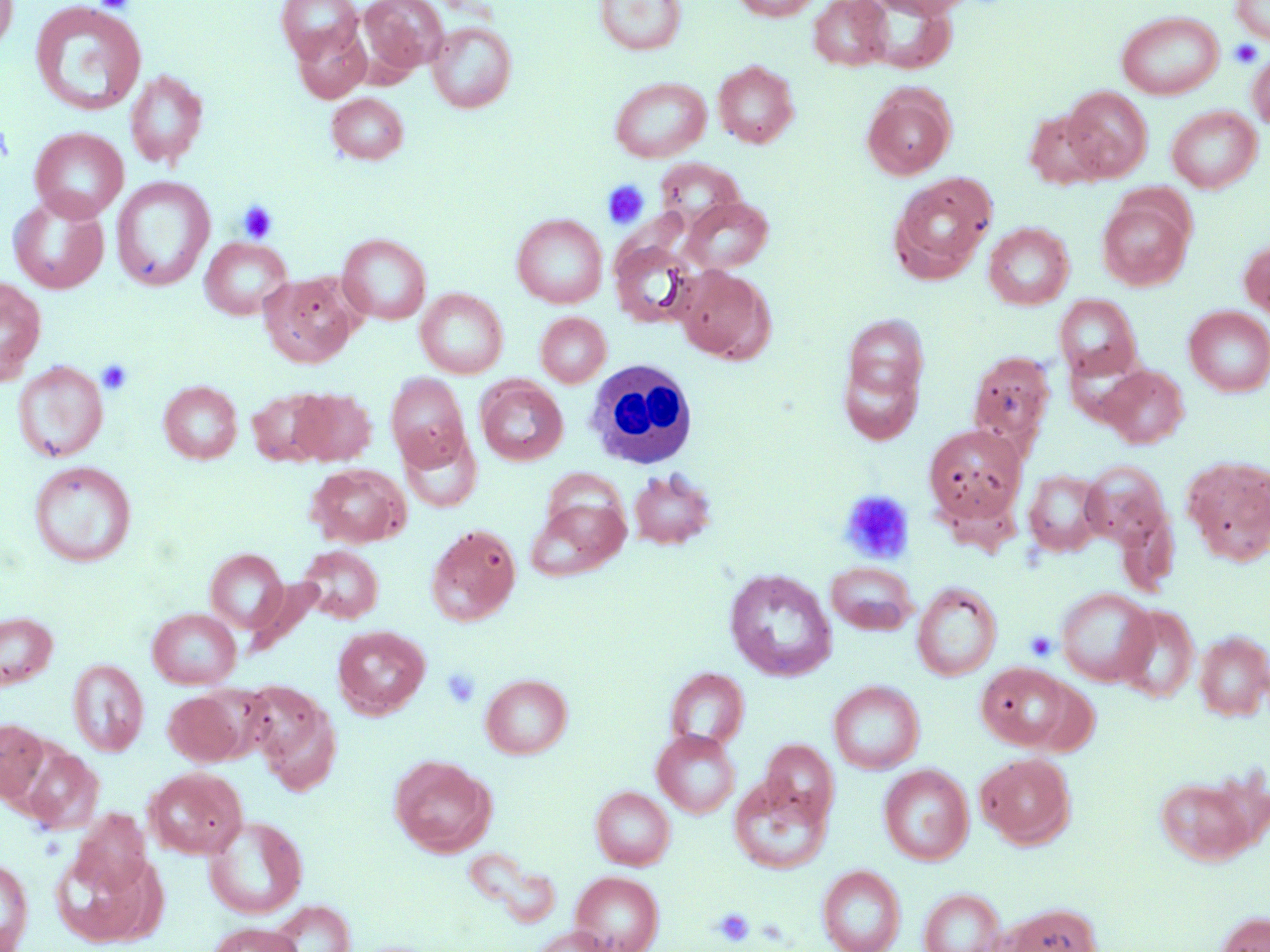
Summary:
  - Coordinate format: approximate bounding boxes as (x1,y1)-(x2,y2) corner pairs in pixels
  - Uninfected red blood cell locations: (0,0)-(18,54), (360,0)-(447,73), (594,0)-(687,56), (731,0)-(821,21), (809,0)-(891,70), (868,0)-(976,18), (1232,0)-(1270,44), (30,1)-(147,117), (277,1)-(363,62), (1116,10)-(1224,100), (427,22)-(517,113), (292,25)-(371,103), (1247,46)-(1270,131), (713,60)-(799,148), (124,68)-(208,169), (610,77)-(711,162), (862,84)-(956,179), (1062,86)-(1152,180), (326,93)-(408,164), (1166,106)-(1262,193), (1024,110)-(1109,189), (29,128)-(128,222), (655,158)-(746,232), (889,172)-(996,283), (111,177)-(215,292), (1097,193)-(1194,291), (8,194)-(110,294), (682,196)-(774,273), (511,214)-(608,308), (983,222)-(1074,309), (338,233)-(431,324), (200,237)-(292,320), (609,238)-(703,328), (1240,238)-(1269,323), (674,265)-(776,364), (260,272)-(360,368), (0,276)-(46,385), (416,288)-(508,378), (1055,294)-(1143,382), (1184,306)-(1270,397), (536,312)-(611,387), (840,312)-(929,416), (967,350)-(1057,455), (12,360)-(109,463), (1099,365)-(1189,448), (386,373)-(470,468), (476,377)-(568,466), (158,381)-(242,464), (290,388)-(376,465), (248,389)-(332,466), (923,424)-(1027,525), (399,427)-(483,514), (1182,456)-(1270,565), (28,461)-(136,567), (1080,461)-(1173,553), (307,463)-(411,548), (628,468)-(717,549), (1023,469)-(1107,556), (526,496)-(629,582), (425,524)-(521,626), (298,546)-(383,624), (205,548)-(289,634), (825,561)-(918,635), (724,568)-(837,681), (246,577)-(325,655), (912,582)-(1002,681), (1055,587)-(1157,687), (1115,605)-(1200,703), (147,608)-(241,689), (0,611)-(58,690), (332,625)-(430,718), (1194,630)-(1270,721), (68,659)-(148,756), (976,663)-(1075,750), (664,667)-(750,750), (480,674)-(573,758), (1024,678)-(1100,755), (828,680)-(925,774), (244,681)-(340,793), (163,690)-(247,765), (0,718)-(49,803), (652,729)-(740,818), (761,739)-(839,824), (18,744)-(104,834), (975,752)-(1075,849), (390,755)-(495,856), (879,764)-(973,865), (145,767)-(247,858), (1153,770)-(1266,865), (728,774)-(833,875), (590,786)-(675,870), (71,809)-(151,895), (203,815)-(308,919), (49,848)-(167,948), (0,857)-(34,952), (817,865)-(906,952), (570,871)-(664,952), (919,888)-(1007,952), (266,900)-(355,952), (1006,903)-(1100,952), (1214,912)-(1270,952), (207,922)-(303,951), (531,926)-(619,952)
  - White blood cell locations: (582,359)-(699,470)
  - Platelet locations: (94,1)-(135,13), (1229,39)-(1264,68), (0,121)-(14,166), (602,180)-(649,229), (237,200)-(277,244), (96,359)-(134,395), (839,490)-(914,564), (1024,631)-(1058,661), (442,667)-(481,709), (713,907)-(755,947)
  - Slide-level diagnosis: no evidence of blood parasites
  - Magnification: 1000x
  - Stain: May-Grünwald-Giemsa
  - Field of view: single
  - Preparation: thin blood smear
  - Image size: 1270×952 pixels
  - Modality: light microscopy